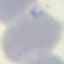

{
  "result": "no malaria parasites detected",
  "preparation": "thin blood smear",
  "stain": "Giemsa",
  "image_type": "automatically extracted cell patch, resized to 64 × 64 pixels",
  "capture": "smartphone through the microscope eyepiece"
}